Outline platelets.
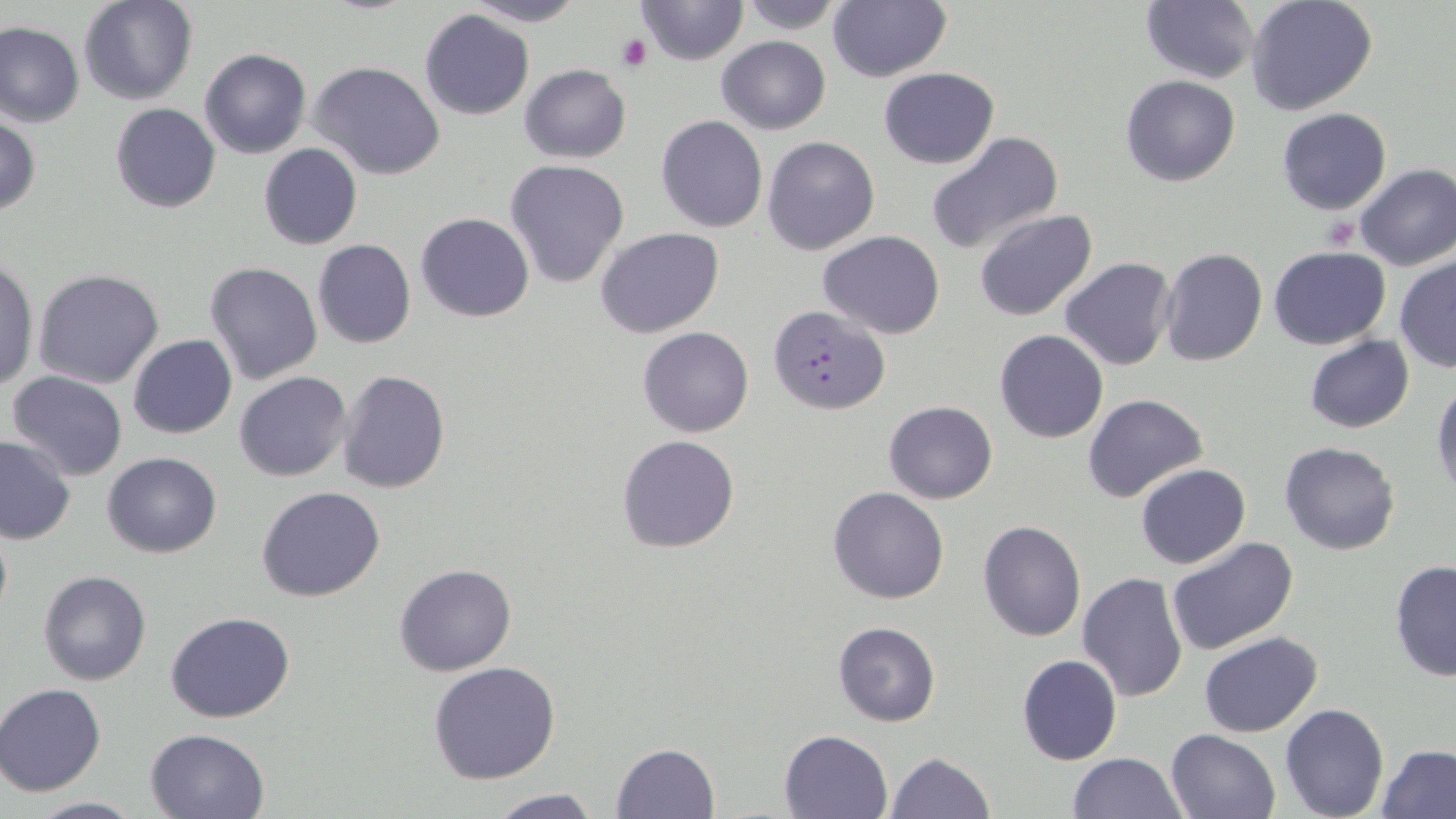
Approximate bounding boxes as (x1,y1)-(x2,y2) corner pairs in pixels.
Platelets: (617,34)-(651,71), (1320,216)-(1360,250).

Plasmodium falciparum-infected red blood cell locations = approximate bounding boxes as (x1,y1)-(x2,y2) corner pairs in pixels: (768,305)-(889,413)
slide-level diagnosis = Plasmodium falciparum
preparation = thin blood film
uninfected red blood cell locations = approximate bounding boxes as (x1,y1)-(x2,y2) corner pairs in pixels: (77,0)-(199,106), (635,0)-(748,66), (732,0)-(850,34), (1247,0)-(1378,116), (465,1)-(586,26), (1141,1)-(1259,85), (827,2)-(950,82), (420,11)-(534,121), (1,22)-(84,127), (715,35)-(832,135), (199,48)-(311,159), (309,61)-(446,180), (518,63)-(631,163), (879,67)-(999,168), (1120,75)-(1240,187), (110,102)-(221,213), (1276,108)-(1392,214), (0,113)-(41,216), (655,114)-(768,234), (924,132)-(1064,256), (762,136)-(880,255), (258,143)-(363,250), (504,159)-(629,288), (1354,163)-(1456,270), (972,208)-(1098,321), (416,212)-(534,322), (596,227)-(724,339), (818,231)-(946,339), (314,241)-(417,350), (1267,246)-(1391,351), (1159,248)-(1267,366), (1394,256)-(1456,375), (1060,258)-(1176,370), (0,259)-(38,392), (204,262)-(323,384), (32,269)-(165,390), (638,327)-(754,438), (994,329)-(1108,444), (128,334)-(237,439), (1305,334)-(1414,433), (6,370)-(128,480), (337,370)-(451,494), (234,371)-(352,482), (1431,379)-(1456,502), (1083,393)-(1209,502), (884,400)-(998,503), (0,434)-(76,544), (616,434)-(741,554), (1280,440)-(1400,555), (102,451)-(221,558), (1135,462)-(1251,568), (256,486)-(386,602), (829,487)-(948,604), (0,518)-(12,630), (978,520)-(1086,642), (1166,537)-(1300,657), (1096,540)-(1253,681), (1389,560)-(1456,682), (394,564)-(517,677), (38,569)-(151,687), (1078,571)-(1190,704), (166,612)-(295,723), (833,622)-(941,727), (1199,631)-(1322,737), (1017,654)-(1122,765), (428,661)-(560,784), (1,683)-(106,796), (1280,703)-(1389,819), (144,727)-(269,818), (1166,728)-(1279,818), (780,731)-(891,816), (609,742)-(722,819), (1377,745)-(1456,819), (886,751)-(994,818), (1067,753)-(1187,818), (482,789)-(604,818), (22,795)-(142,818)
magnification = 1000x
field of view = single
image size = 1456×819 pixels
modality = optical microscopy
stain = May-Grünwald-Giemsa